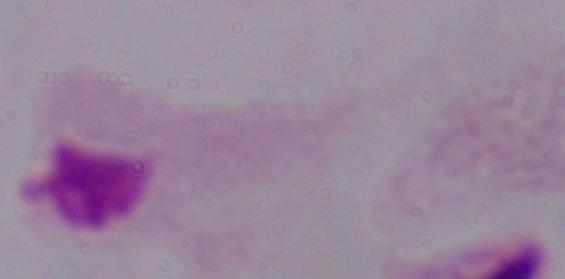

Photomicrograph. A trichomonad is shown. Captured at 1000x magnification.